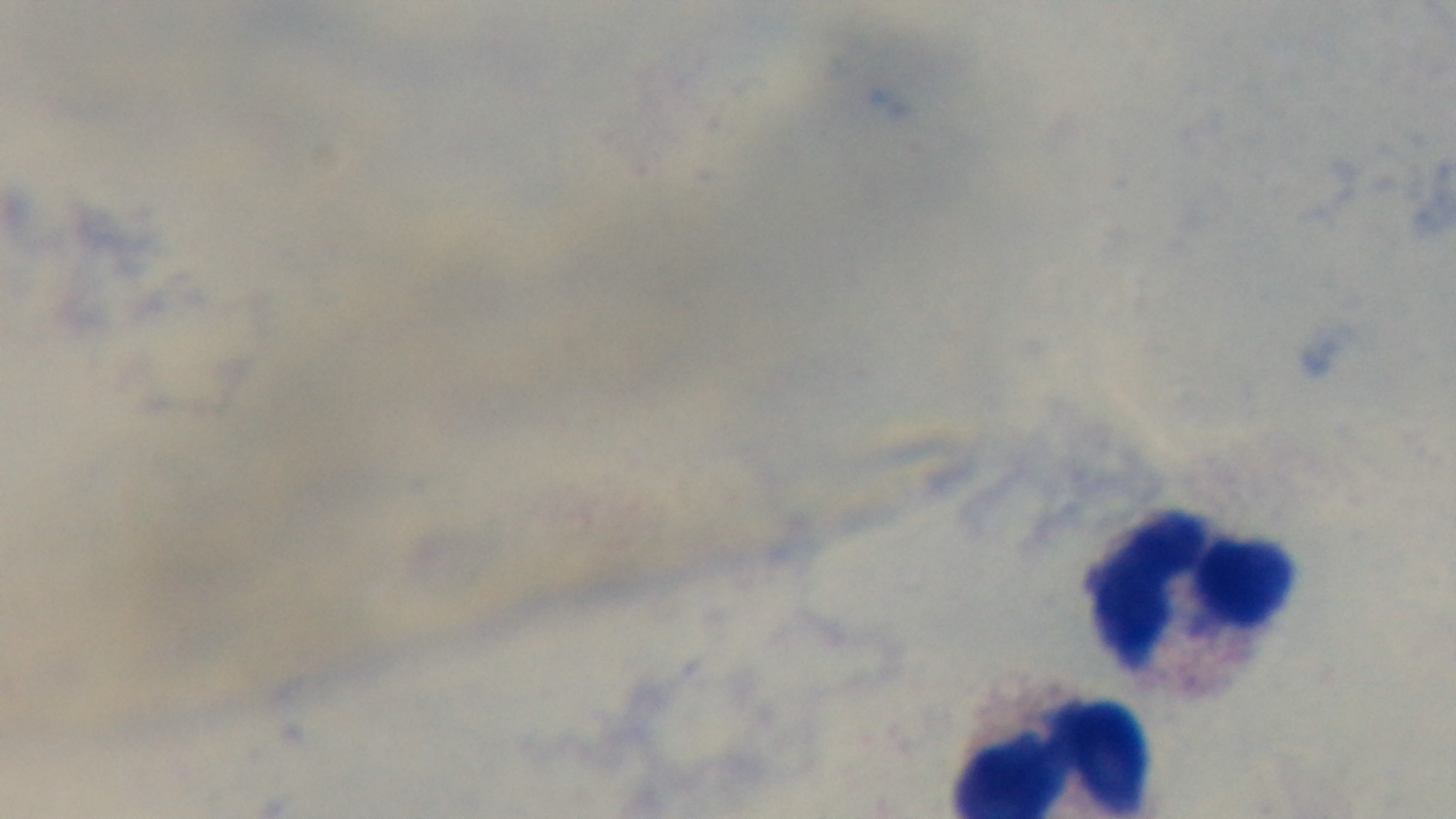
Summary:
  - Capture: mounted 4K digital camera
  - Field of view: one from the slide
  - Stain: Giemsa
  - Preparation: thick blood film
  - Malaria status: uninfected
  - Objective: 100x oil immersion
  - Modality: light microscopy